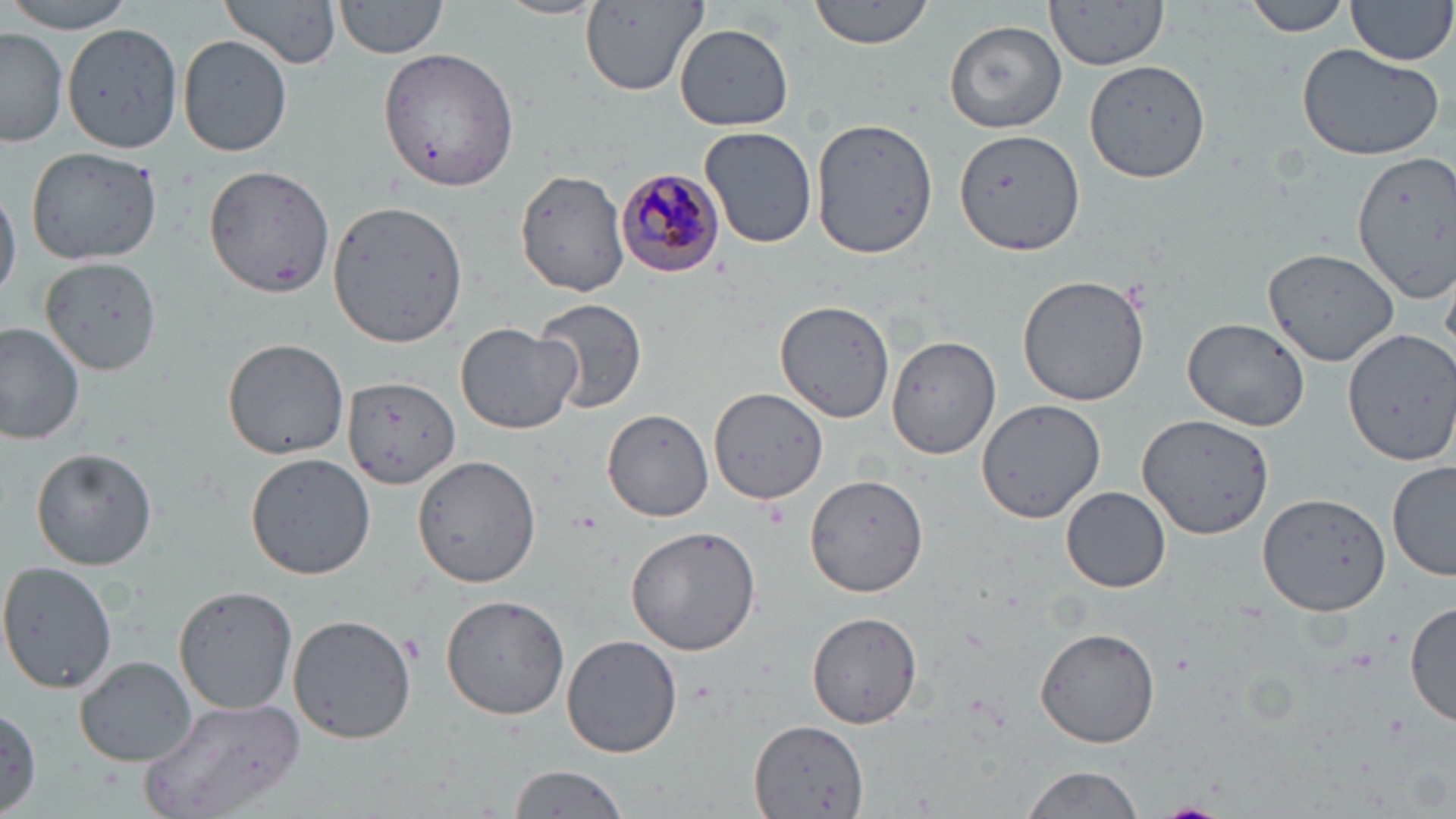

Approximate bounding boxes as named x1/y1/x2/y2 corners in pixels. Uninfected red blood cell locations: (x1=220, y1=0, x2=343, y2=71), (x1=495, y1=0, x2=605, y2=21), (x1=809, y1=0, x2=936, y2=49), (x1=1044, y1=0, x2=1169, y2=71), (x1=1242, y1=0, x2=1354, y2=36), (x1=1347, y1=0, x2=1455, y2=67), (x1=0, y1=1, x2=140, y2=31), (x1=334, y1=1, x2=449, y2=62), (x1=580, y1=1, x2=704, y2=95), (x1=945, y1=18, x2=1067, y2=133), (x1=60, y1=22, x2=183, y2=152), (x1=674, y1=23, x2=794, y2=129), (x1=1, y1=28, x2=67, y2=149), (x1=178, y1=34, x2=293, y2=157), (x1=1296, y1=43, x2=1447, y2=161), (x1=376, y1=48, x2=520, y2=192), (x1=1084, y1=60, x2=1209, y2=183), (x1=811, y1=118, x2=938, y2=257), (x1=698, y1=126, x2=817, y2=249), (x1=954, y1=127, x2=1086, y2=256), (x1=26, y1=145, x2=164, y2=264), (x1=1352, y1=150, x2=1456, y2=301), (x1=204, y1=165, x2=334, y2=297), (x1=515, y1=169, x2=629, y2=298), (x1=0, y1=189, x2=20, y2=302), (x1=324, y1=200, x2=468, y2=347), (x1=1265, y1=247, x2=1397, y2=364), (x1=39, y1=259, x2=158, y2=380), (x1=1017, y1=274, x2=1150, y2=406), (x1=532, y1=297, x2=648, y2=414), (x1=775, y1=300, x2=896, y2=424), (x1=1182, y1=317, x2=1312, y2=433), (x1=0, y1=322, x2=83, y2=445), (x1=455, y1=323, x2=583, y2=434), (x1=1343, y1=327, x2=1455, y2=466), (x1=888, y1=336, x2=1000, y2=460), (x1=222, y1=337, x2=348, y2=460), (x1=344, y1=376, x2=459, y2=491), (x1=708, y1=389, x2=829, y2=504), (x1=977, y1=399, x2=1105, y2=523), (x1=602, y1=410, x2=714, y2=522), (x1=1136, y1=413, x2=1274, y2=540), (x1=31, y1=446, x2=158, y2=571), (x1=244, y1=453, x2=374, y2=579), (x1=413, y1=455, x2=541, y2=588), (x1=1387, y1=457, x2=1455, y2=581), (x1=805, y1=472, x2=932, y2=596), (x1=1062, y1=487, x2=1171, y2=593), (x1=1257, y1=492, x2=1392, y2=614), (x1=625, y1=527, x2=761, y2=655), (x1=0, y1=560, x2=117, y2=695), (x1=174, y1=583, x2=299, y2=716), (x1=440, y1=593, x2=570, y2=720), (x1=1407, y1=600, x2=1456, y2=729), (x1=806, y1=610, x2=924, y2=729), (x1=290, y1=612, x2=418, y2=743), (x1=1034, y1=628, x2=1160, y2=748), (x1=562, y1=635, x2=682, y2=758), (x1=76, y1=655, x2=198, y2=767), (x1=139, y1=695, x2=305, y2=819), (x1=1, y1=703, x2=41, y2=817), (x1=752, y1=719, x2=869, y2=818), (x1=506, y1=764, x2=630, y2=819), (x1=1017, y1=766, x2=1145, y2=819). Plasmodium malariae-infected red blood cell locations: (x1=615, y1=166, x2=725, y2=276). Slide-level diagnosis: Plasmodium malariae. Optical microscopy. One field of a larger specimen. May-Grünwald-Giemsa-stained preparation. 1000x magnification. Image is 1456×819 pixels. Thin blood smear.